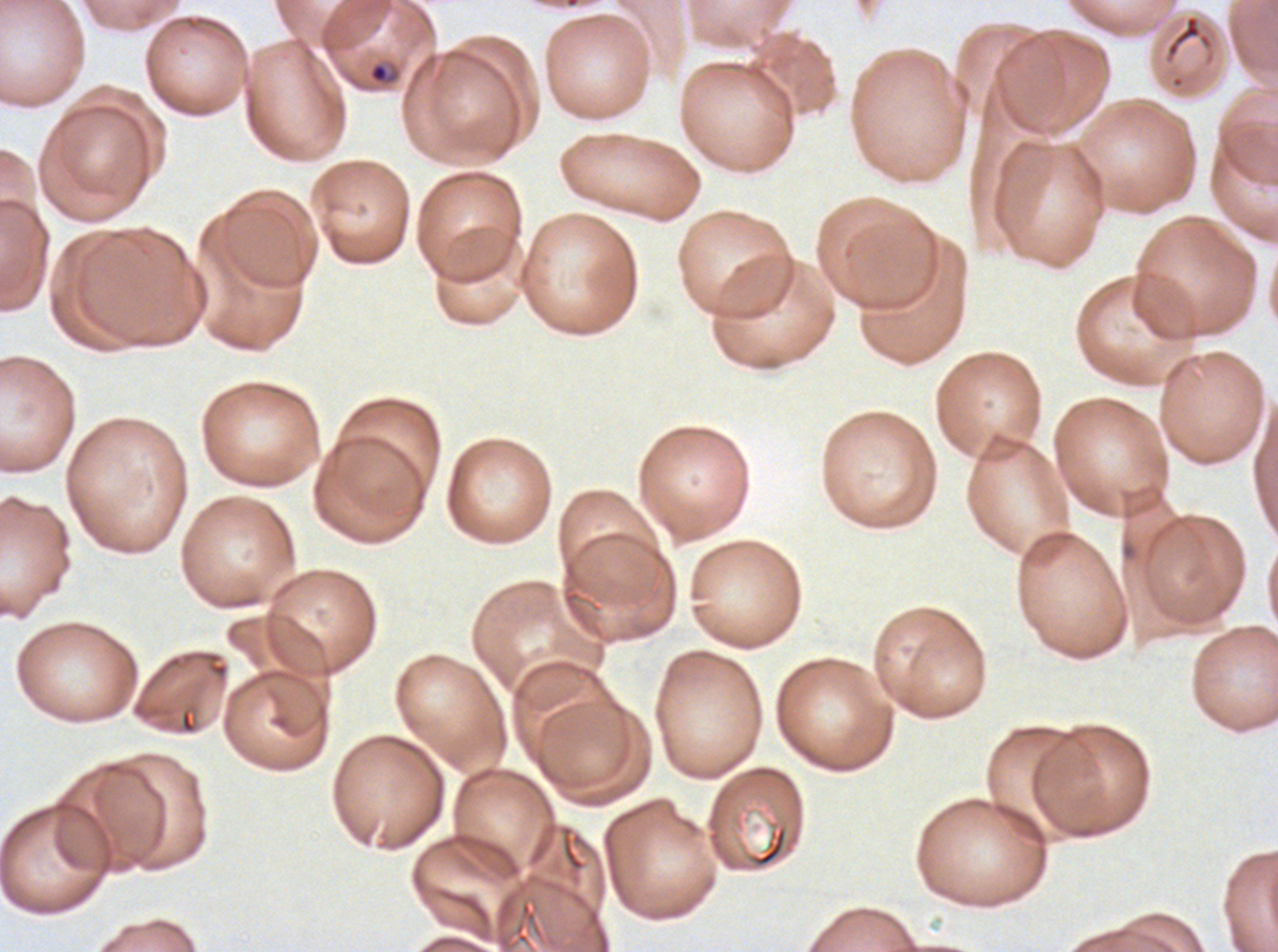

Approximate bounding boxes as [x1, y1, x2, y2] in pixels.
Summary:
  - Ring locations: [367, 61, 399, 85]
  - Debris locations: [1163, 13, 1214, 64], [748, 824, 789, 869]
  - Image size: 1278×952 pixels
  - Specimen: Plasmodium falciparum from a patient in The Gambia, cultured ex vivo for 24 to 48 hours
  - Stain: Giemsa
  - Preparation: thin blood smear
  - Field of view: one sub-image of a larger composite